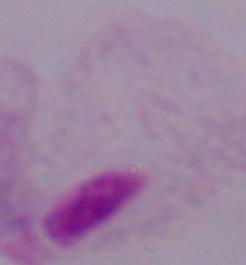
Summary:
  - Magnification: 1000x
  - Identification: trichomonad
  - Modality: photomicrograph